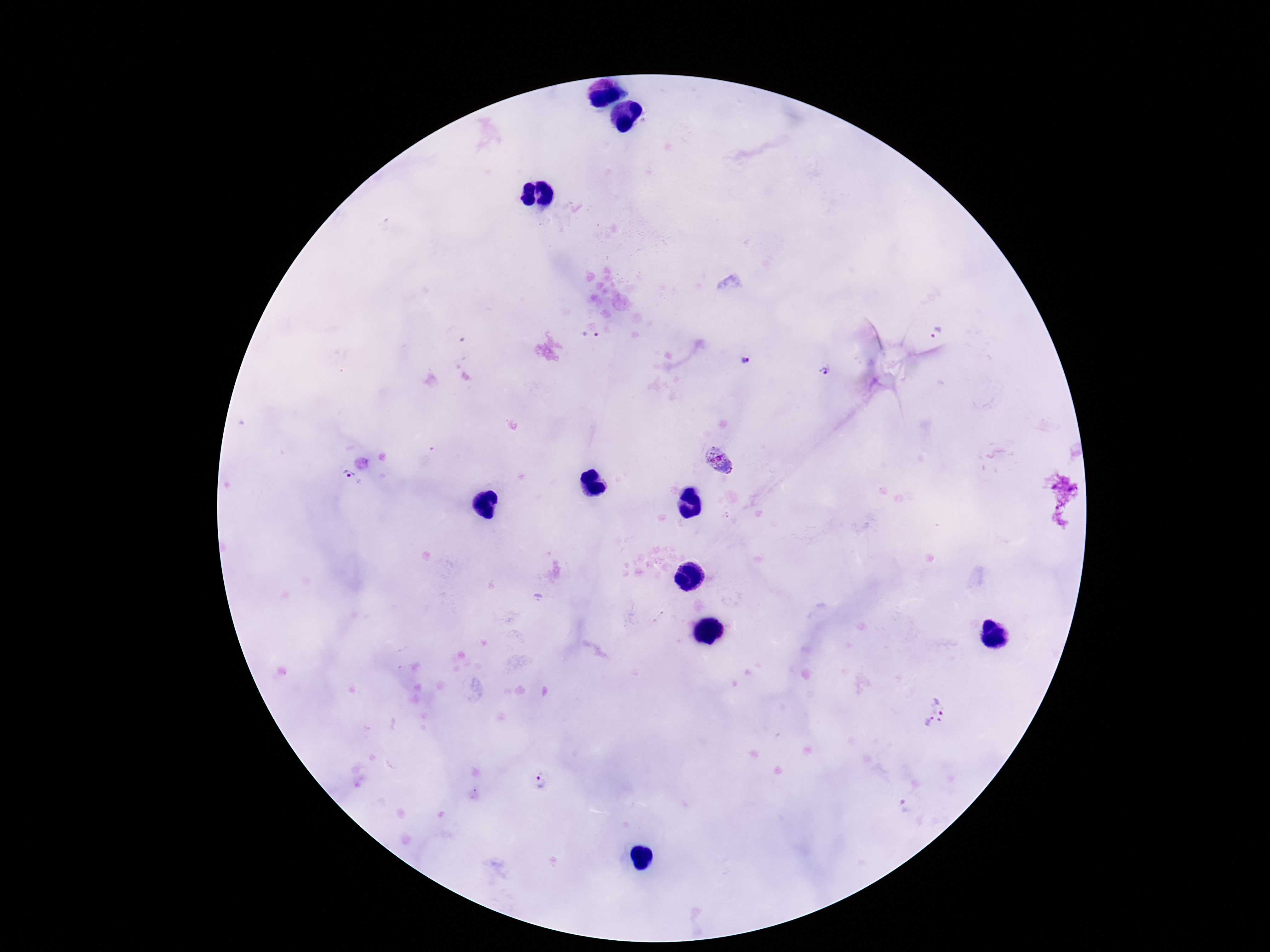
Approximate centers as (x, y) in pixels.
Summary:
  - Plasmodium parasite locations: (938, 333), (590, 337), (745, 360), (824, 371), (720, 462), (350, 484), (725, 518), (934, 712), (542, 783), (907, 808)
  - Magnification: 100x
  - Patient malaria status: infected
  - Capture: smartphone camera through the microscope eyepiece
  - Preparation: thick peripheral-blood smear
  - Field of view: one from this slide
  - Stain: Giemsa
  - Image size: 1270×952 pixels